Name the parasite shown.
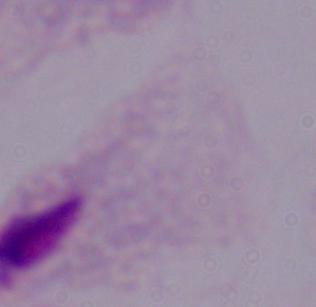
A trichomonad.

Captured at 1000x magnification. Photomicrograph.